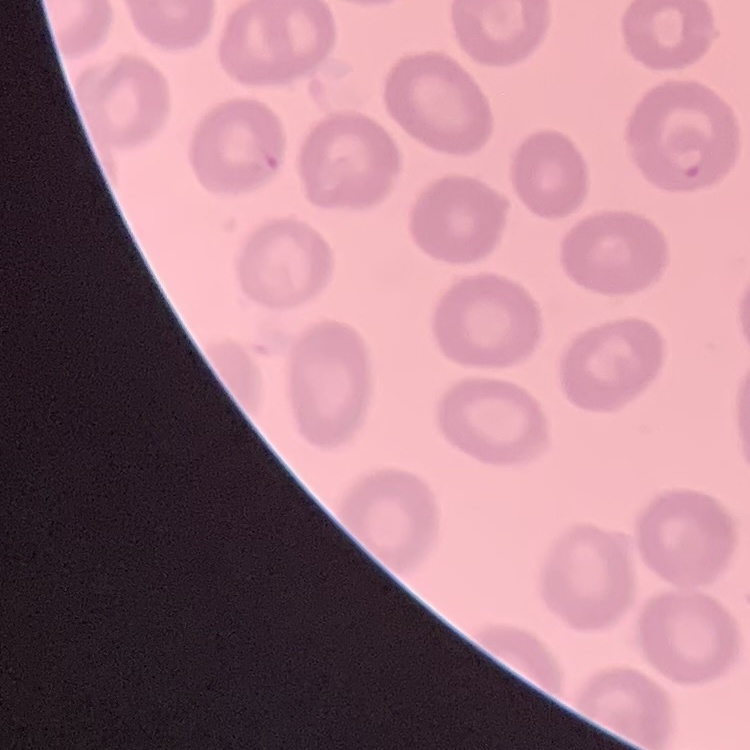

red blood cell morphology = no rouleaux formation
image type = one tile cut from a larger photomicrograph
stain = Field's or Giemsa
preparation = thin peripheral smear